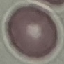
{
  "result": "no malaria parasites detected",
  "preparation": "thin blood smear",
  "image_type": "cell patch, automatically extracted from a larger field of view and resized to 64 × 64 pixels",
  "capture": "smartphone through the microscope eyepiece",
  "stain": "Giemsa"
}